State which parasite is depicted.
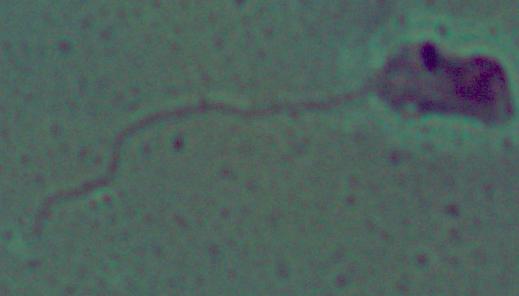
This is Leishmania.

1000x magnification. Micrograph.